Give the extent of all Plasmodium ovale-infected red blood cells.
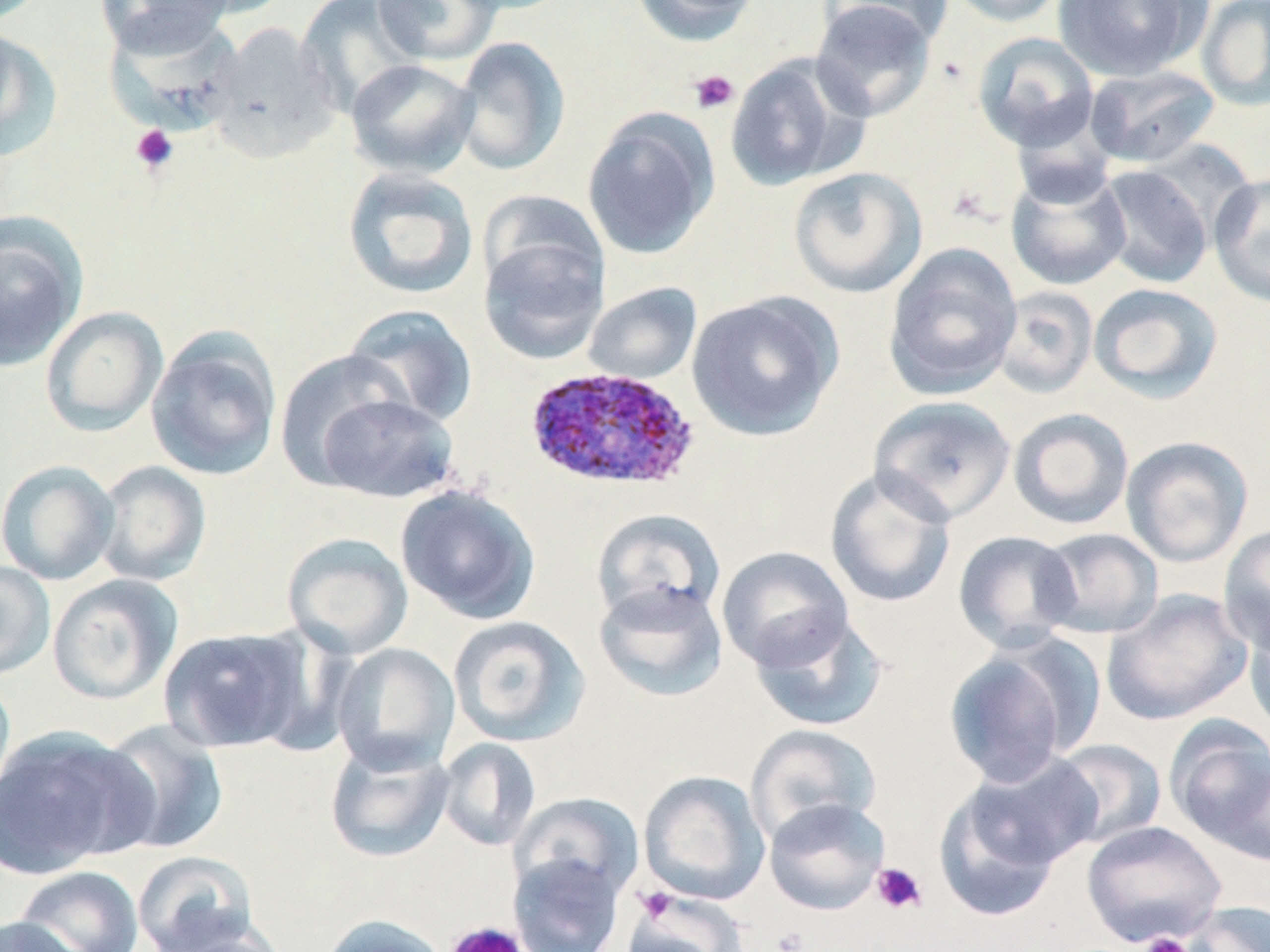
Approximate bounding boxes as (x1,y1)-(x2,y2) corner pairs in pixels.
Plasmodium ovale-infected red blood cells: (523,366)-(701,492).

slide-level diagnosis = Plasmodium ovale
stain = May-Grünwald-Giemsa
image size = 1270×952 pixels
uninfected red blood cell locations = approximate bounding boxes as (x1,y1)-(x2,y2) corner pairs in pixels: (96,0)-(237,56), (371,0)-(501,66), (447,0)-(576,16), (629,0)-(763,47), (824,0)-(950,49), (944,0)-(1069,27), (1053,0)-(1208,81), (1197,0)-(1270,112), (295,1)-(423,117), (809,1)-(937,121), (99,16)-(243,135), (207,21)-(340,163), (0,24)-(63,163), (972,31)-(1100,152), (452,36)-(570,177), (724,54)-(867,192), (345,58)-(480,179), (1084,65)-(1220,167), (582,108)-(720,261), (1095,165)-(1214,288), (787,166)-(928,298), (1006,166)-(1131,291), (342,167)-(479,300), (1209,173)-(1270,308), (476,189)-(608,308), (0,216)-(86,373), (478,228)-(609,364), (882,244)-(1024,400), (583,282)-(702,385), (1088,283)-(1224,403), (993,286)-(1098,399), (686,292)-(844,442), (342,304)-(478,429), (40,305)-(168,436), (145,328)-(283,481), (275,349)-(414,489), (313,388)-(460,503), (870,395)-(1016,524), (1008,408)-(1134,530), (1121,435)-(1254,568), (0,459)-(120,585), (93,460)-(212,586), (824,467)-(957,608), (395,484)-(542,624), (591,507)-(726,627), (1218,524)-(1270,655), (1036,527)-(1164,639), (953,529)-(1082,653), (282,532)-(413,659), (716,546)-(854,670), (0,560)-(55,680), (47,573)-(184,705), (594,580)-(728,702), (1101,588)-(1253,726), (748,610)-(890,732), (1244,614)-(1270,740), (447,615)-(590,746), (158,626)-(310,753), (942,641)-(1087,787), (331,642)-(460,774), (0,672)-(16,810), (1165,717)-(1270,855), (96,719)-(229,856), (745,723)-(882,845), (0,725)-(151,878), (324,738)-(455,863), (437,738)-(541,852), (1049,739)-(1168,850), (960,753)-(1103,873), (638,770)-(770,906), (934,782)-(1064,923), (510,792)-(643,904), (762,798)-(891,915), (1081,820)-(1226,946), (132,850)-(259,952), (507,852)-(625,952), (13,865)-(145,952), (623,890)-(749,952), (1180,901)-(1269,952), (316,914)-(451,952), (0,916)-(88,952), (153,927)-(290,951)
preparation = thin blood smear
field of view = single
platelet locations = approximate bounding boxes as (x1,y1)-(x2,y2) corner pairs in pixels: (688,69)-(739,115), (130,124)-(178,175), (870,861)-(928,915), (633,886)-(680,925), (444,921)-(529,952), (1138,932)-(1194,952)
magnification = 1000x
modality = optical microscopy